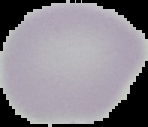
Summary:
  - Image type: cell region segmented out of the field of view; surrounding area masked to black
  - Preparation: thin blood smear
  - Image size: 148×127 pixels
  - Malaria status: uninfected